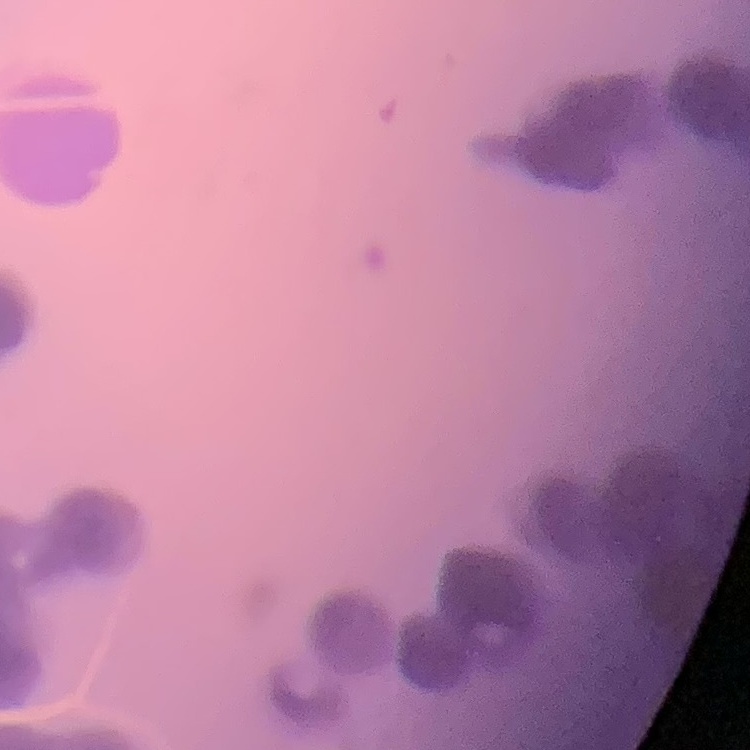
Summary:
  - Erythrocyte morphology: rouleaux formation
  - Stain: Field's or Giemsa
  - Image type: square crop of a larger photomicrograph
  - Preparation: thin peripheral smear